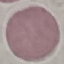 Result: negative for malaria parasites. Thin blood smear. Acquired by smartphone through the microscope eyepiece. Cell patch, automatically extracted from a larger field of view and resized to 64 × 64 pixels. Giemsa stain.